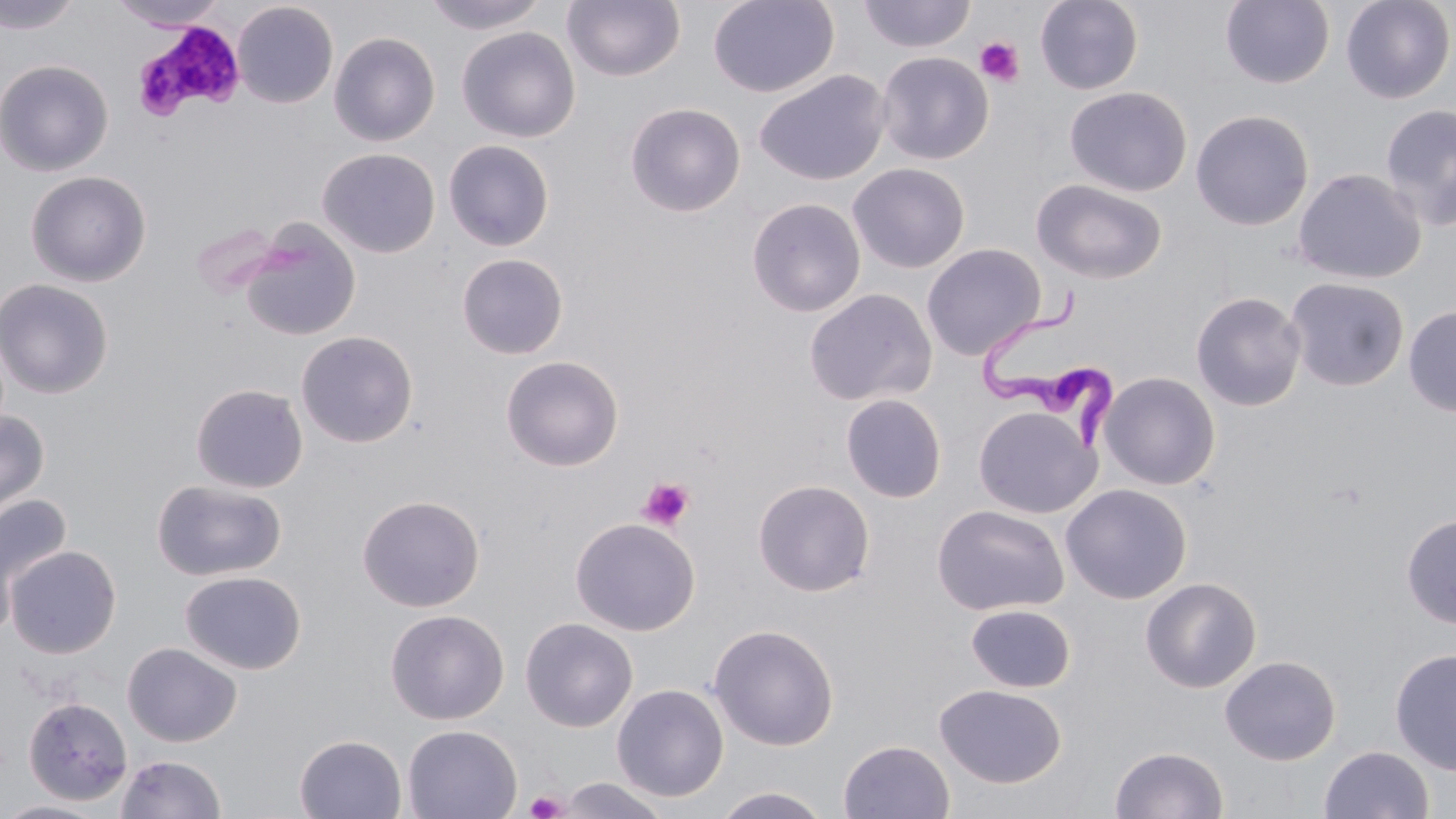

Approximate bounding boxes as (x1,y1)-(x2,y2) corner pairs in pixels. Platelet locations: (137,21)-(245,119), (975,36)-(1026,87), (636,476)-(695,532), (525,790)-(569,819). Trypanosoma brucei locations: (977,283)-(1118,452). Uninfected red blood cell locations: (0,0)-(84,34), (421,0)-(551,35), (708,0)-(839,97), (857,0)-(976,53), (1034,0)-(1144,95), (1220,0)-(1334,89), (1341,0)-(1454,104), (110,1)-(227,31), (562,1)-(686,82), (232,2)-(339,108), (456,26)-(580,143), (329,31)-(440,146), (875,51)-(994,165), (0,59)-(113,177), (753,69)-(891,186), (1064,86)-(1192,197), (625,102)-(746,217), (1379,104)-(1456,231), (1190,110)-(1314,231), (443,139)-(555,251), (318,148)-(440,258), (847,163)-(970,273), (1292,168)-(1426,285), (26,171)-(151,287), (1031,179)-(1168,284), (746,198)-(866,317), (241,219)-(362,341), (921,243)-(1046,361), (456,253)-(569,360), (1285,277)-(1410,392), (1,278)-(114,399), (803,288)-(938,407), (1190,291)-(1307,411), (1403,306)-(1456,417), (296,331)-(418,448), (500,355)-(624,471), (1099,371)-(1221,490), (190,384)-(309,493), (840,393)-(947,503), (973,405)-(1099,519), (0,408)-(50,522), (151,479)-(287,582), (753,479)-(875,597), (1060,483)-(1193,604), (1,491)-(72,613), (357,494)-(485,612), (931,504)-(1069,617), (1401,513)-(1456,629), (570,517)-(700,636), (4,545)-(122,658), (180,570)-(307,674), (1140,576)-(1262,693), (965,604)-(1076,692), (385,609)-(509,725), (520,617)-(638,732), (707,623)-(839,750), (122,642)-(242,747), (1389,648)-(1456,776), (1219,654)-(1341,766), (612,683)-(730,802), (934,683)-(1067,788), (22,695)-(133,806), (402,724)-(522,819), (294,734)-(407,818), (838,739)-(955,819), (1320,745)-(1434,818), (1110,746)-(1229,819), (115,754)-(227,818), (556,777)-(673,819), (711,786)-(834,819), (0,799)-(111,818). Slide-level diagnosis: Trypanosoma brucei. May-Grünwald-Giemsa-stained preparation. Single field of view. 1000x magnification. Optical microscopy. Thin blood smear. Image is 1456×819 pixels.